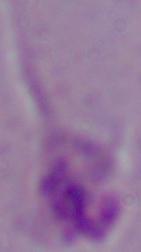
{
  "identification": "Leishmania",
  "modality": "photomicrograph",
  "magnification": "1000x"
}